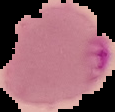
Summary:
  - Image type: cell region segmented out of the field of view; surrounding area masked to black
  - Malaria status: parasitized
  - Preparation: thin blood film
  - Image size: 115×112 pixels